Give the extent of all white blood cells.
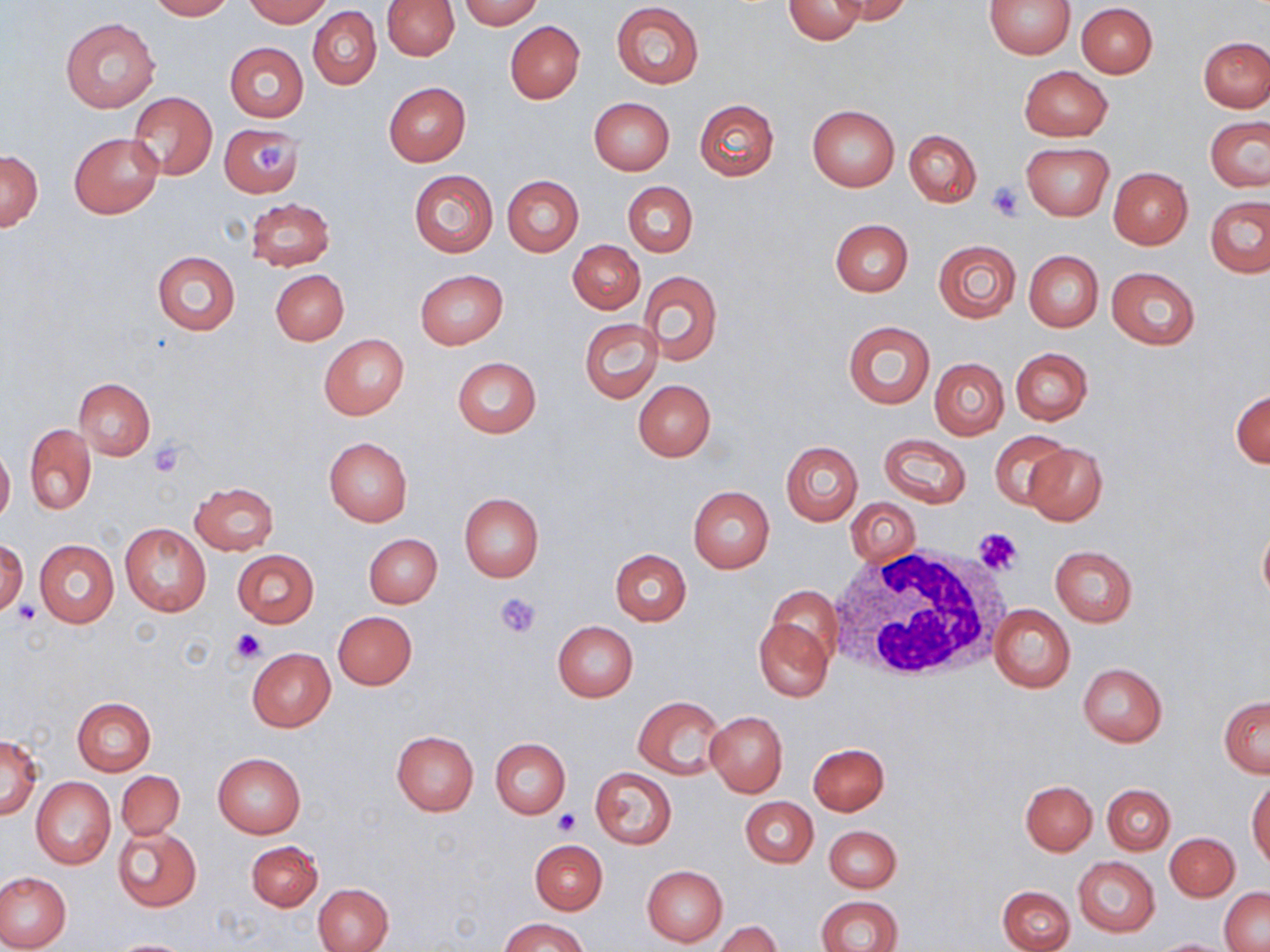
Approximate bounding boxes as (x1, y1, x2, y2) in pixels.
White blood cells: (828, 547, 1010, 686).

{
  "slide_level_diagnosis": "negative for blood parasites",
  "uninfected_red_blood_cell_locations": "approximate bounding boxes as (x1, y1, x2, y2) in pixels: (149, 0, 233, 20), (245, 0, 330, 25), (459, 0, 540, 28), (783, 0, 866, 44), (831, 0, 915, 25), (986, 0, 1076, 58), (383, 1, 460, 59), (611, 2, 704, 88), (1075, 2, 1158, 79), (308, 6, 382, 90), (60, 16, 160, 112), (505, 21, 585, 103), (1199, 35, 1269, 112), (225, 42, 308, 122), (1018, 65, 1112, 140), (384, 83, 470, 166), (128, 91, 216, 181), (588, 98, 674, 176), (694, 99, 779, 181), (807, 105, 900, 191), (1205, 117, 1270, 192), (217, 122, 306, 197), (904, 129, 981, 207), (69, 132, 163, 218), (1022, 143, 1113, 220), (1, 150, 43, 231), (1108, 168, 1192, 250), (408, 169, 499, 257), (503, 176, 583, 257), (623, 182, 697, 256), (1205, 194, 1270, 278), (246, 198, 334, 271), (829, 219, 913, 296), (933, 239, 1022, 322), (568, 240, 643, 313), (152, 249, 240, 336), (1023, 250, 1103, 331), (1106, 266, 1201, 350), (271, 269, 349, 345), (415, 270, 508, 350), (639, 270, 723, 364), (579, 318, 662, 404), (844, 320, 934, 408), (319, 334, 410, 420), (1010, 347, 1092, 425), (929, 357, 1008, 440), (452, 358, 540, 438), (74, 378, 155, 460), (633, 379, 716, 461), (1231, 387, 1269, 469), (24, 424, 96, 514), (991, 430, 1074, 509), (878, 433, 971, 508), (324, 437, 412, 525), (782, 441, 863, 525), (1023, 443, 1108, 526), (0, 444, 14, 524), (190, 482, 278, 555), (687, 487, 775, 572), (459, 492, 544, 581), (846, 498, 920, 567), (1257, 521, 1270, 607), (121, 523, 211, 617), (364, 534, 442, 607), (34, 539, 120, 628), (0, 540, 27, 615), (1050, 545, 1138, 626), (610, 548, 692, 626), (232, 549, 318, 628), (765, 587, 842, 676), (990, 603, 1075, 692), (334, 611, 417, 689), (753, 616, 834, 703), (552, 620, 638, 701), (247, 648, 334, 731), (1077, 663, 1167, 746), (633, 695, 726, 780), (1219, 696, 1269, 776), (73, 697, 155, 776), (706, 711, 787, 797), (391, 731, 478, 815), (0, 737, 42, 818), (490, 738, 570, 818), (807, 743, 889, 815), (212, 753, 305, 840), (590, 767, 677, 849), (116, 771, 185, 841), (31, 777, 115, 869), (1248, 777, 1269, 869), (1020, 780, 1097, 855), (1102, 784, 1175, 854), (740, 796, 818, 867), (114, 825, 201, 911), (824, 825, 901, 892), (1167, 833, 1239, 900), (529, 841, 607, 914), (246, 842, 322, 911), (1073, 855, 1160, 937), (642, 865, 727, 946), (0, 873, 71, 950), (314, 883, 392, 951), (999, 885, 1074, 952), (1220, 887, 1270, 950), (816, 895, 902, 952), (501, 917, 587, 952), (714, 921, 782, 952), (108, 938, 197, 951), (1149, 938, 1234, 952)",
  "modality": "optical microscopy",
  "image_size": "1270×952 pixels",
  "preparation": "thin blood film",
  "magnification": "1000x",
  "platelet_locations": "approximate bounding boxes as (x1, y1, x2, y2) in pixels: (252, 137, 291, 176), (987, 183, 1023, 221), (147, 442, 186, 477), (976, 528, 1025, 575), (495, 591, 544, 637), (10, 602, 38, 626), (230, 629, 267, 664), (554, 808, 580, 834)",
  "stain": "May-Grünwald-Giemsa",
  "field_of_view": "single"
}